State which cell type is depicted.
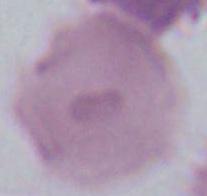
An erythrocyte.

Photomicrograph. Captured at 1000x magnification.